Name the parasite shown.
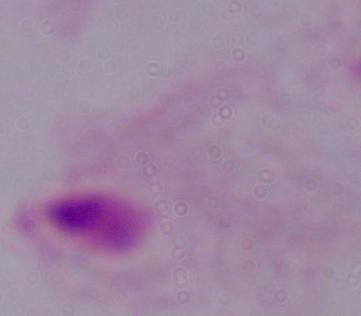

A trichomonad.

Photomicrograph. 1000x magnification.